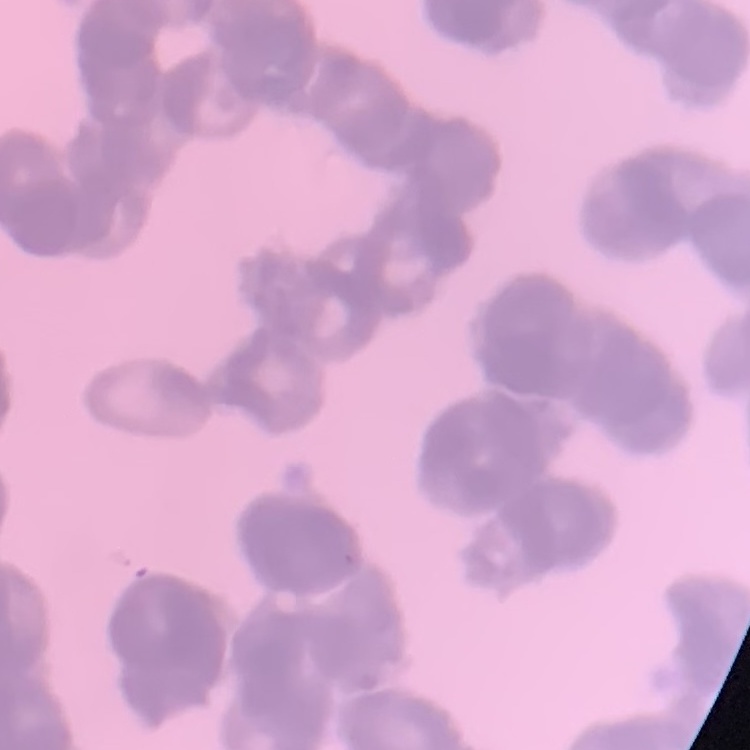
Summary:
  - Red blood cell morphology: rouleaux formation
  - Preparation: thin peripheral smear
  - Image type: square crop of a larger photomicrograph
  - Stain: Field's or Giemsa